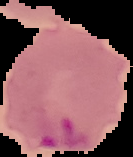

malaria status = parasitized
preparation = thin blood smear
image type = segmented cell region with the area outside set to black
image size = 133×157 pixels